Identify the blood parasite species.
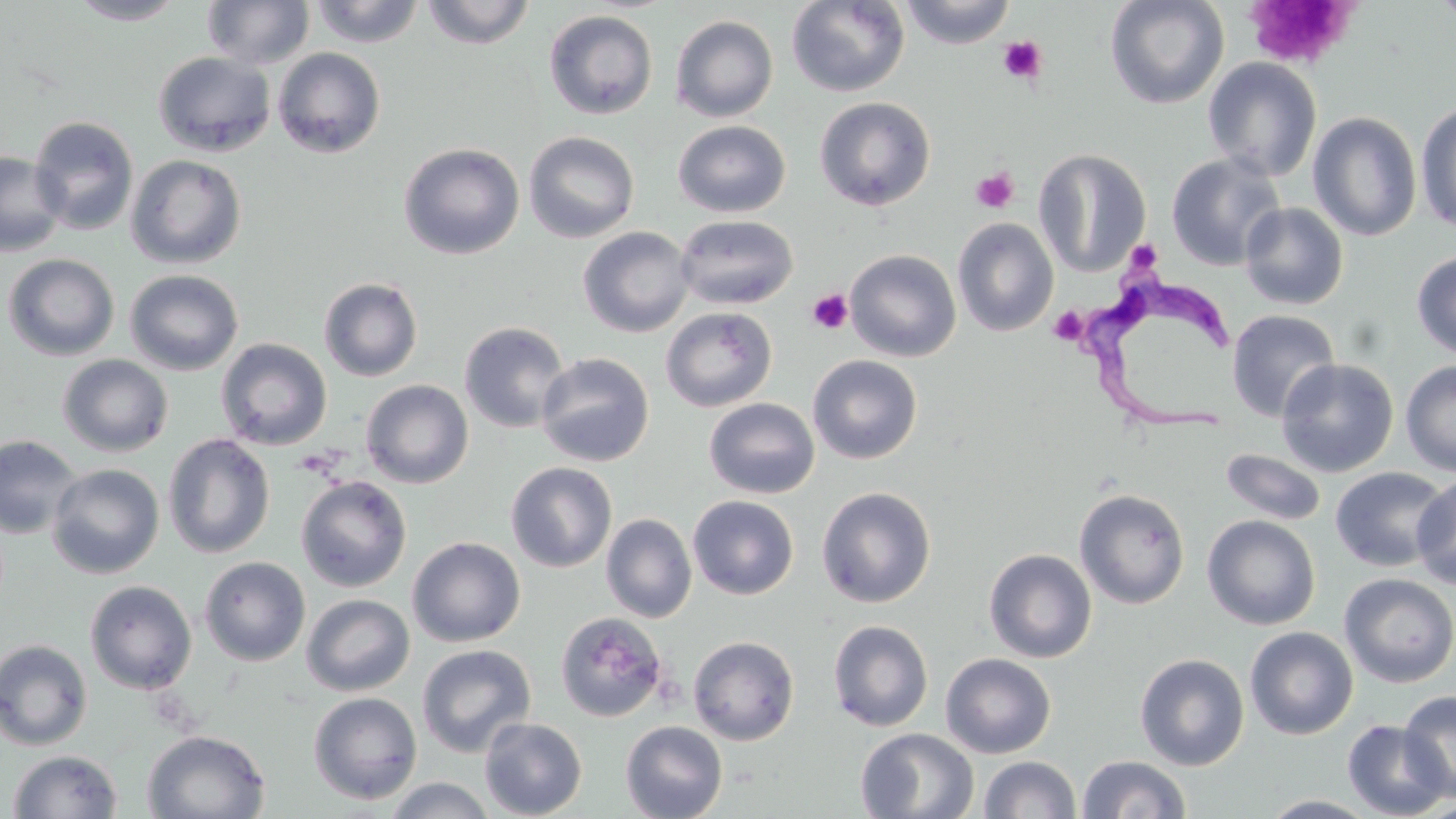
Trypanosoma brucei.

Approximate bounding boxes as (x1,y1)-(x2,y2) corner pairs in pixels. Platelet locations: (1244,1)-(1359,72), (998,36)-(1048,85), (970,167)-(1019,214), (1130,239)-(1166,275), (806,288)-(853,334), (1048,307)-(1087,345). Trypanosoma brucei locations: (1085,275)-(1251,439). Uninfected red blood cell locations: (67,0)-(188,25), (309,0)-(425,47), (420,0)-(536,49), (786,0)-(910,97), (899,0)-(1017,48), (1104,0)-(1230,110), (1432,0)-(1456,28), (202,1)-(315,69), (544,9)-(659,120), (670,15)-(779,122), (272,47)-(387,159), (153,51)-(276,157), (1202,57)-(1323,182), (814,96)-(936,211), (1416,100)-(1456,236), (1307,112)-(1422,242), (28,115)-(140,235), (673,120)-(791,217), (523,130)-(639,243), (398,142)-(525,260), (1033,148)-(1152,277), (0,151)-(66,257), (1166,153)-(1287,271), (126,154)-(247,269), (1240,202)-(1349,310), (674,214)-(799,310), (953,218)-(1058,336), (577,226)-(695,338), (845,249)-(961,361), (1411,250)-(1456,361), (2,253)-(120,361), (125,269)-(244,376), (319,276)-(423,382), (661,307)-(777,412), (1226,309)-(1340,422), (459,321)-(571,433), (496,334)-(625,448), (216,338)-(333,451), (535,352)-(655,467), (810,353)-(925,463), (57,354)-(174,457), (1276,358)-(1399,478), (1400,359)-(1456,477), (361,380)-(473,488), (704,398)-(820,499), (163,433)-(276,559), (0,434)-(83,540), (1220,449)-(1327,526), (506,461)-(617,572), (47,463)-(165,579), (1329,466)-(1452,572), (296,475)-(412,592), (1412,475)-(1456,591), (816,486)-(937,608), (1074,488)-(1190,608), (688,495)-(799,600), (601,513)-(697,623), (1202,515)-(1320,630), (407,536)-(525,648), (983,549)-(1097,663), (200,556)-(310,666), (1339,573)-(1456,688), (85,580)-(197,694), (301,594)-(415,696), (557,612)-(668,723), (827,619)-(933,731), (1244,626)-(1358,739), (688,635)-(800,746), (0,639)-(93,751), (417,644)-(537,758), (941,652)-(1056,759), (1134,653)-(1249,771), (1398,690)-(1456,802), (308,691)-(423,804), (479,717)-(587,818), (1342,719)-(1452,818), (620,721)-(727,819), (855,728)-(979,818), (142,729)-(271,818), (7,750)-(123,819), (1077,754)-(1191,818), (979,755)-(1080,817), (382,777)-(496,818), (1258,795)-(1385,818). May-Grünwald-Giemsa stain. 1000x magnification. Image is 1456×819 pixels. Thin blood film. One field of a larger specimen. Light microscopy.